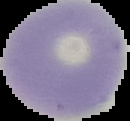
preparation = thin blood film
malaria status = uninfected
image type = cell region segmented out of the field of view; surrounding area masked to black
image size = 130×121 pixels